Identify the parasite.
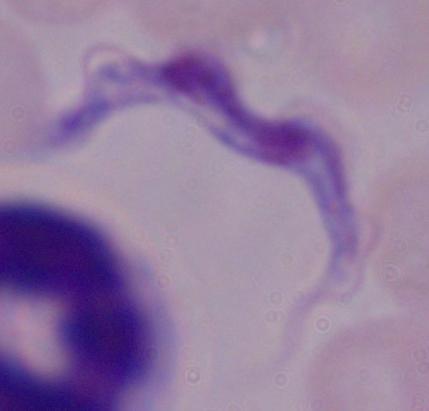
A trypanosome.

modality = photomicrograph
magnification = 1000x